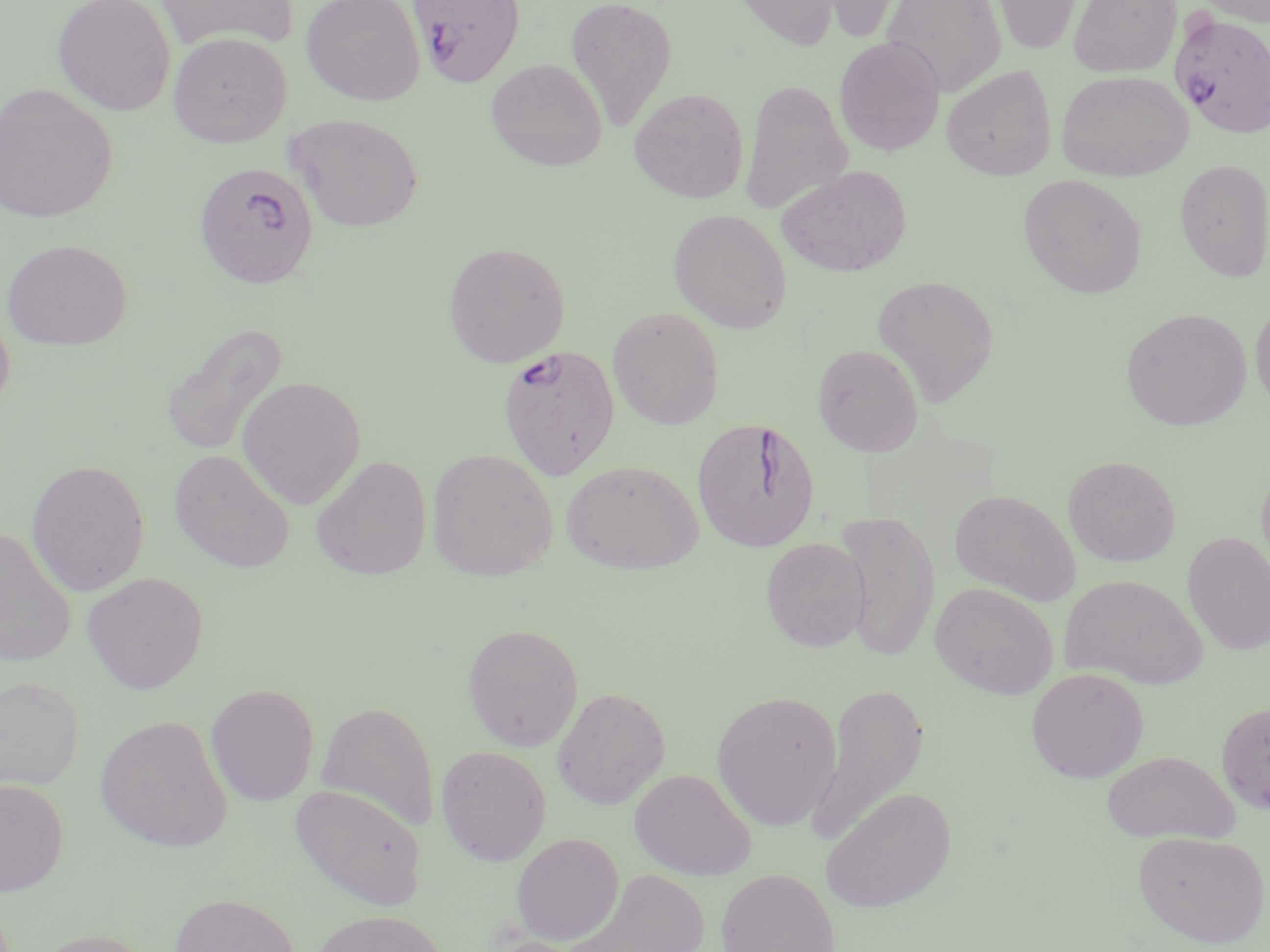
Approximate bounding boxes as (x1, y1, x2, y2) in pixels. Uninfected red blood cell locations: (52, 0, 177, 116), (155, 0, 300, 53), (300, 0, 426, 106), (565, 0, 679, 132), (731, 0, 841, 51), (808, 0, 916, 43), (882, 0, 1007, 98), (991, 0, 1085, 55), (1068, 0, 1182, 78), (1195, 0, 1270, 27), (167, 31, 292, 147), (833, 35, 945, 155), (485, 58, 607, 171), (940, 64, 1057, 181), (1056, 70, 1193, 181), (740, 79, 853, 217), (0, 83, 118, 224), (629, 87, 749, 203), (285, 113, 425, 233), (1174, 158, 1270, 281), (776, 164, 912, 278), (1017, 173, 1148, 298), (667, 209, 792, 334), (1, 238, 133, 350), (442, 241, 571, 368), (871, 274, 1000, 406), (1250, 298, 1270, 414), (0, 300, 15, 418), (607, 306, 725, 429), (1121, 307, 1252, 431), (159, 320, 290, 460), (812, 343, 924, 456), (236, 375, 367, 510), (169, 448, 296, 573), (426, 448, 559, 582), (310, 455, 432, 581), (1062, 455, 1181, 567), (25, 458, 150, 597), (1256, 458, 1270, 585), (560, 459, 704, 574), (949, 488, 1081, 606), (831, 510, 941, 662), (0, 525, 77, 668), (1181, 531, 1270, 656), (760, 537, 870, 652), (81, 571, 209, 694), (1059, 574, 1208, 688), (930, 581, 1059, 700), (462, 622, 584, 751), (1026, 666, 1149, 783), (0, 674, 85, 791), (205, 683, 320, 807), (811, 683, 930, 846), (552, 686, 671, 809), (711, 689, 843, 830), (315, 700, 440, 833), (1216, 701, 1270, 816), (94, 713, 233, 853), (434, 744, 552, 866), (1100, 750, 1240, 844), (629, 768, 757, 880), (0, 777, 69, 896), (289, 784, 427, 911), (820, 786, 956, 914), (1131, 830, 1269, 948), (511, 833, 624, 946), (715, 867, 840, 952), (563, 869, 711, 952), (167, 892, 302, 952), (308, 909, 451, 952), (25, 927, 158, 952). Plasmodium falciparum-infected red blood cell locations: (408, 0, 525, 88), (1169, 10, 1270, 141), (197, 162, 324, 292), (497, 344, 620, 479), (691, 417, 822, 553). Slide-level diagnosis: Plasmodium falciparum. Light microscopy. One field of a larger specimen. Thin blood smear. 1000x magnification. Image is 1270×952 pixels. May-Grünwald-Giemsa-stained preparation.